Describe the morphology of the red blood cells.
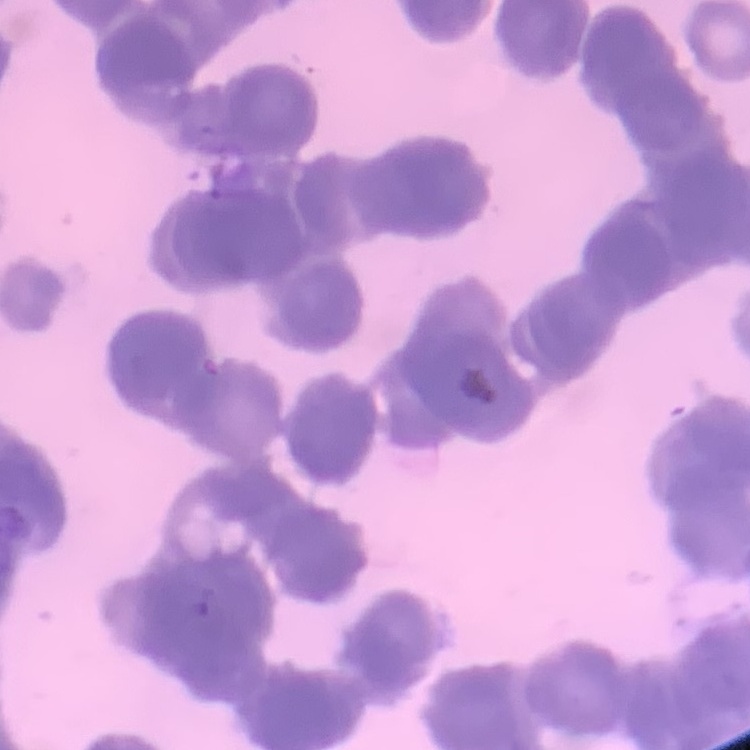

Rouleaux formation.

Thin peripheral smear. Square crop of a larger photomicrograph. Field's or Giemsa stain.